Outline each blood parasite and name the species.
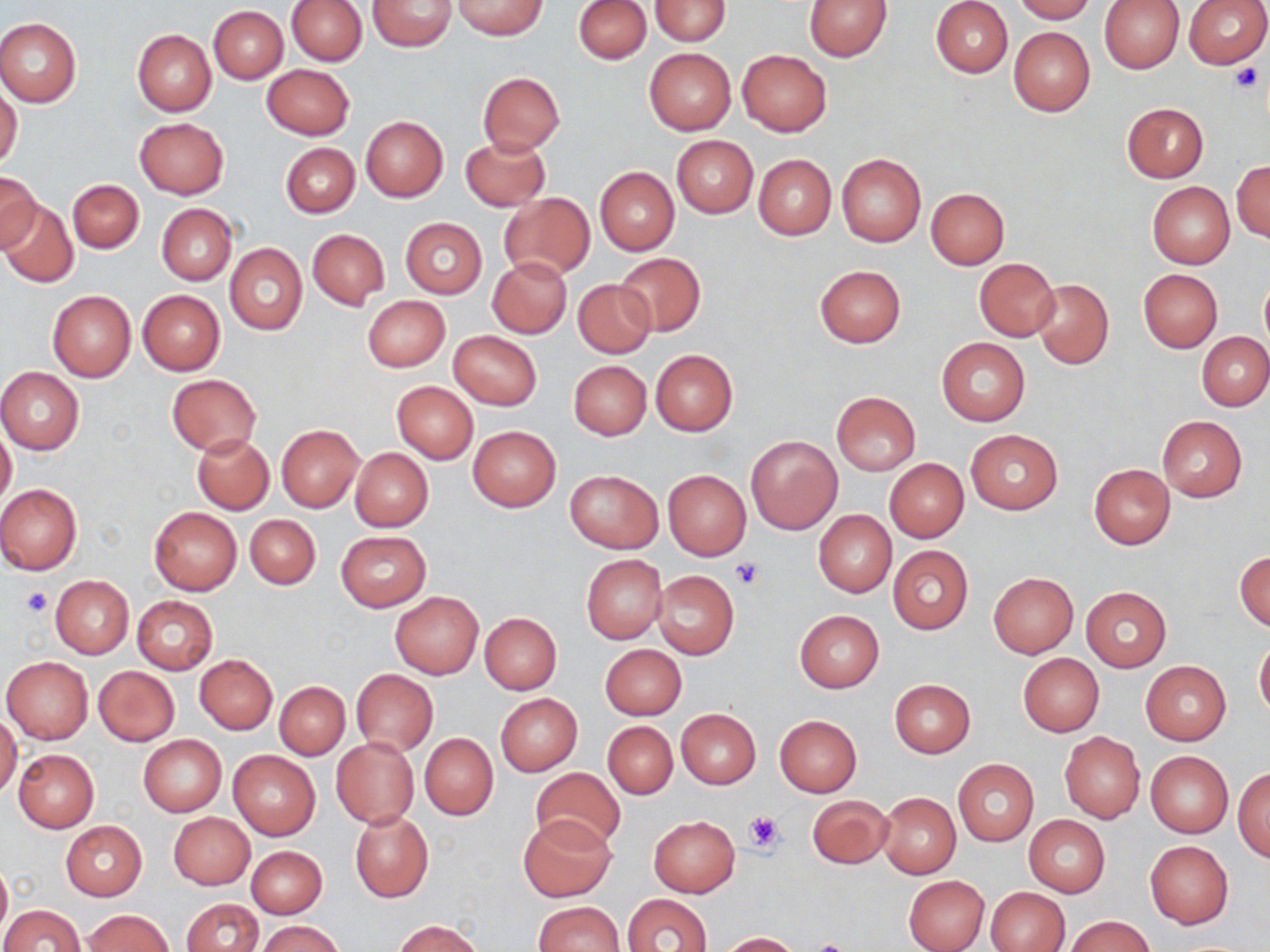
No blood parasites observed.

Approximate bounding boxes as [x1, y1, x2, y2] in pixels. Platelet locations: [1231, 62, 1263, 92], [731, 558, 765, 589], [22, 586, 51, 616], [743, 809, 787, 853], [805, 940, 858, 952]. Uninfected red blood cell locations: [367, 0, 456, 51], [649, 0, 730, 45], [931, 0, 1012, 77], [1010, 0, 1096, 22], [1183, 0, 1270, 68], [287, 1, 367, 64], [451, 1, 548, 39], [574, 1, 651, 63], [803, 1, 891, 61], [1099, 1, 1184, 74], [209, 6, 288, 83], [0, 19, 82, 106], [1008, 26, 1095, 117], [132, 29, 216, 117], [644, 47, 736, 135], [737, 50, 831, 136], [262, 64, 354, 139], [478, 72, 565, 154], [0, 86, 23, 171], [1122, 102, 1209, 182], [360, 115, 448, 202], [134, 117, 229, 200], [461, 135, 550, 212], [671, 135, 757, 218], [280, 143, 359, 218], [836, 152, 927, 247], [754, 153, 836, 240], [1232, 160, 1270, 242], [595, 166, 679, 255], [0, 171, 40, 250], [67, 179, 143, 253], [1147, 182, 1234, 267], [925, 187, 1009, 268], [499, 193, 594, 281], [3, 201, 78, 288], [156, 204, 236, 285], [400, 217, 487, 299], [306, 228, 389, 309], [225, 244, 307, 334], [614, 252, 707, 337], [488, 258, 572, 338], [975, 259, 1059, 340], [815, 265, 905, 347], [1138, 269, 1222, 352], [1259, 275, 1270, 355], [573, 278, 656, 358], [1031, 278, 1113, 369], [138, 290, 224, 375], [48, 291, 135, 380], [362, 296, 450, 372], [450, 330, 542, 410], [1197, 331, 1270, 411], [937, 338, 1030, 426], [651, 349, 738, 436], [569, 360, 651, 440], [0, 369, 84, 453], [167, 375, 261, 454], [391, 381, 478, 463], [831, 391, 920, 476], [1158, 416, 1247, 501], [276, 424, 364, 512], [0, 425, 16, 509], [467, 426, 560, 512], [965, 429, 1063, 515], [193, 434, 273, 514], [745, 434, 842, 534], [350, 448, 433, 531], [885, 458, 967, 542], [1089, 464, 1175, 549], [565, 470, 662, 552], [663, 470, 751, 560], [0, 484, 82, 574], [149, 506, 242, 595], [814, 511, 896, 597], [245, 514, 321, 590], [336, 531, 430, 611], [888, 545, 974, 634], [1235, 550, 1270, 631], [580, 554, 667, 644], [652, 571, 739, 659], [988, 572, 1078, 657], [50, 575, 133, 658], [627, 586, 728, 686], [1080, 586, 1173, 672], [390, 592, 484, 679], [132, 595, 218, 673], [794, 610, 885, 692], [480, 613, 562, 694], [1255, 638, 1270, 720], [599, 644, 687, 720], [1018, 654, 1104, 736], [3, 655, 93, 743], [195, 655, 277, 733], [1140, 661, 1231, 744], [94, 666, 180, 745], [352, 669, 438, 754], [889, 679, 976, 758], [275, 682, 349, 759], [496, 693, 582, 776], [676, 709, 760, 789], [0, 713, 21, 799], [774, 714, 863, 797], [603, 721, 677, 798], [1059, 731, 1145, 823], [419, 733, 498, 820], [139, 735, 226, 816], [331, 738, 419, 827], [13, 749, 99, 832], [227, 750, 319, 841], [1145, 751, 1233, 836], [953, 759, 1038, 846], [1234, 766, 1270, 861], [531, 768, 626, 851], [878, 793, 960, 879], [808, 795, 894, 868], [350, 811, 433, 902], [169, 813, 254, 889], [519, 813, 616, 902], [648, 816, 740, 896], [1024, 816, 1110, 896], [61, 821, 147, 900], [1145, 841, 1233, 928], [246, 846, 327, 918], [0, 860, 10, 944], [903, 874, 990, 952], [987, 887, 1070, 952], [623, 894, 711, 952], [181, 898, 263, 952], [532, 901, 623, 951], [1, 904, 84, 952], [84, 910, 173, 951], [1067, 916, 1154, 952], [257, 920, 341, 952], [395, 920, 484, 952], [721, 932, 804, 952]. Slide-level diagnosis: no evidence of blood parasites. Single field of view. Light microscopy. Captured at 1000x magnification. Image is 1270×952 pixels. May-Grünwald-Giemsa stain. Thin blood smear.